Evaluate for Plasmodium parasites.
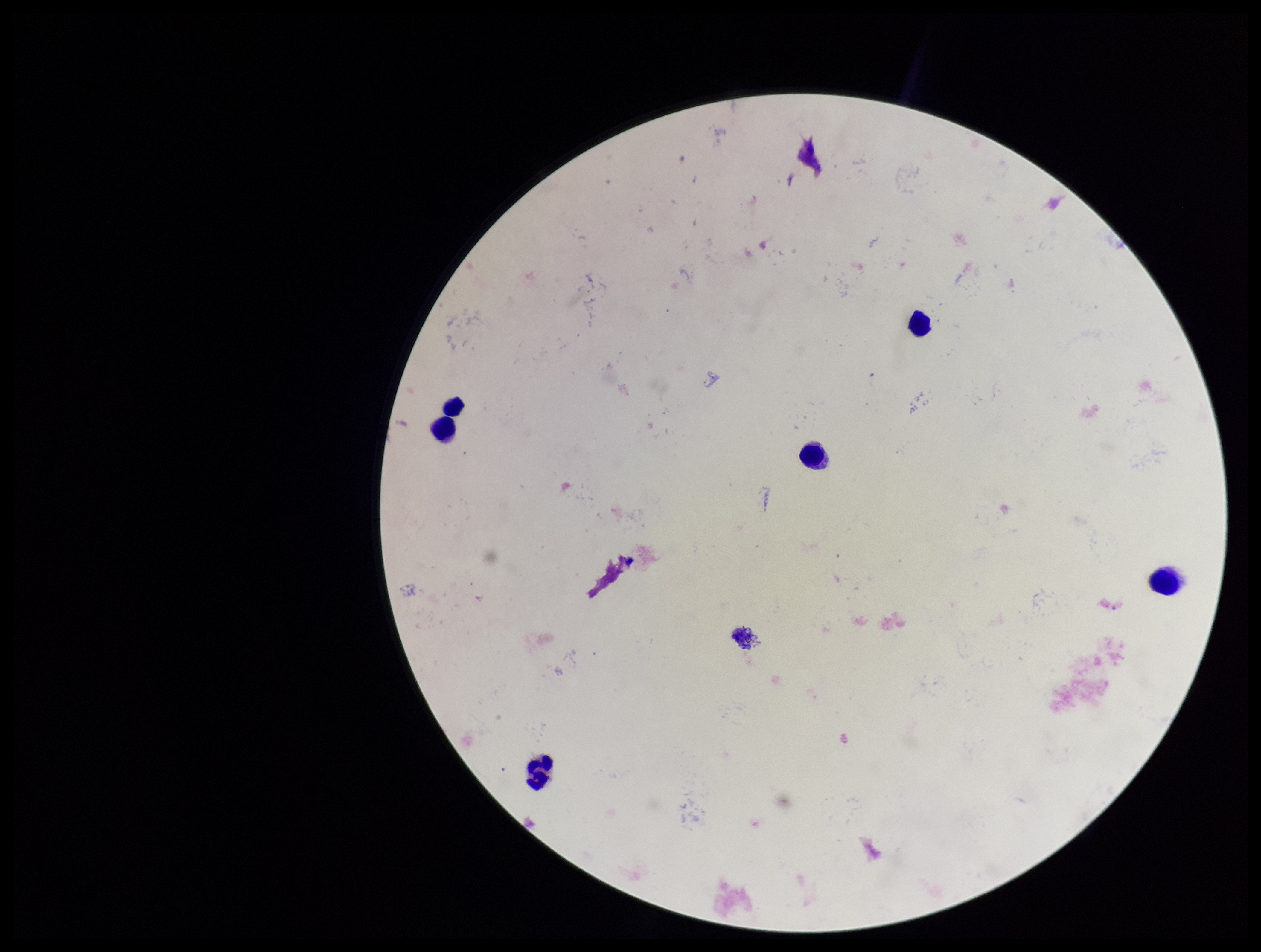

None identified.

Preparation: thick. Patient malaria status: negative. Leukocyte count: 6. Parasite count: 0. Smartphone photograph taken through the eyepiece of a microscope. Giemsa stain. Image is 1261×952 pixels. One field from this slide.